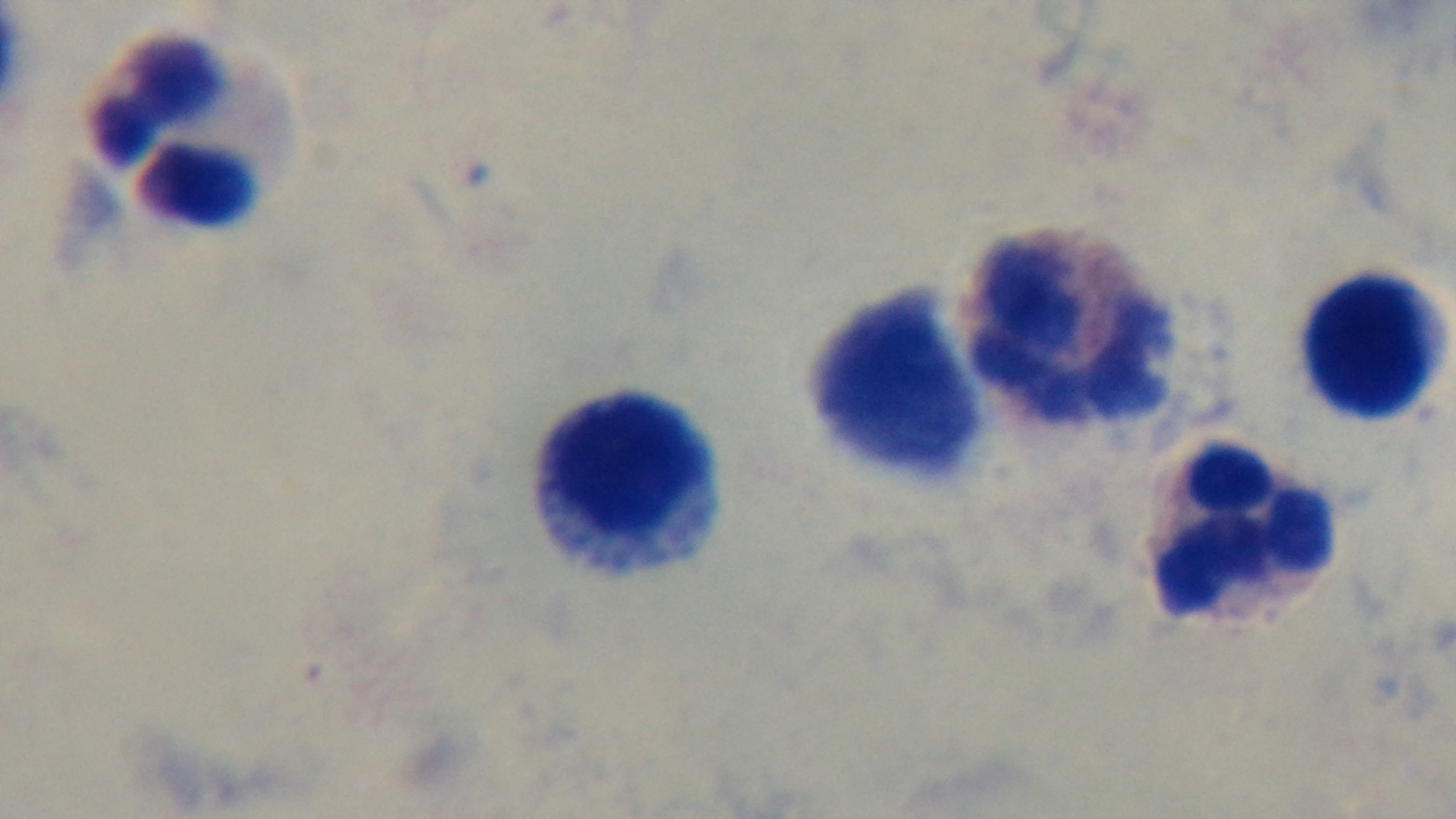
{
  "modality": "light microscopy",
  "capture": "mounted 4K digital camera",
  "field_of_view": "one from the slide",
  "malaria_status": "negative",
  "preparation": "thick",
  "stain": "Giemsa",
  "objective": "100x oil immersion"
}